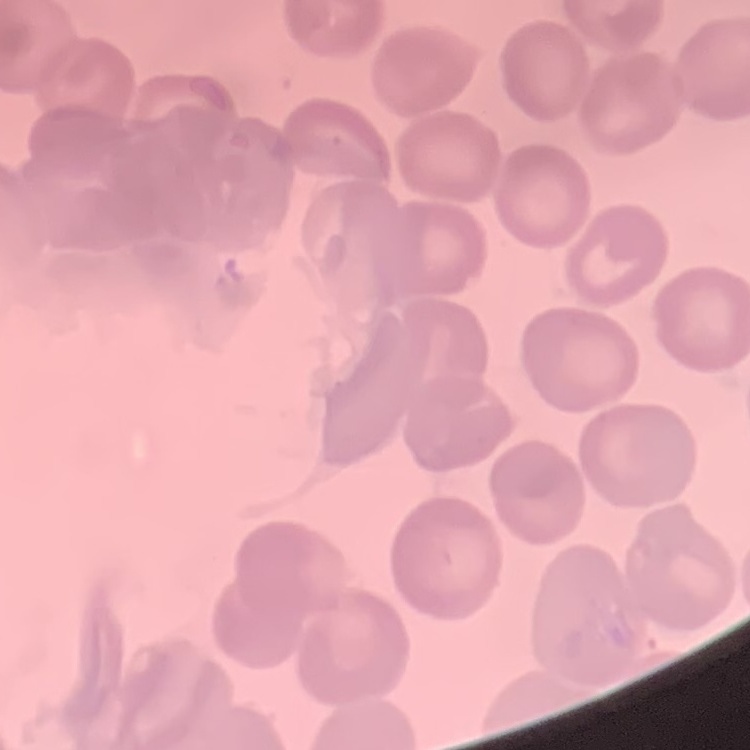
The erythrocytes show no rouleaux formation. Thin blood film. One tile cut from a larger photomicrograph. Field's or Giemsa stain.